Identify the blood parasite species.
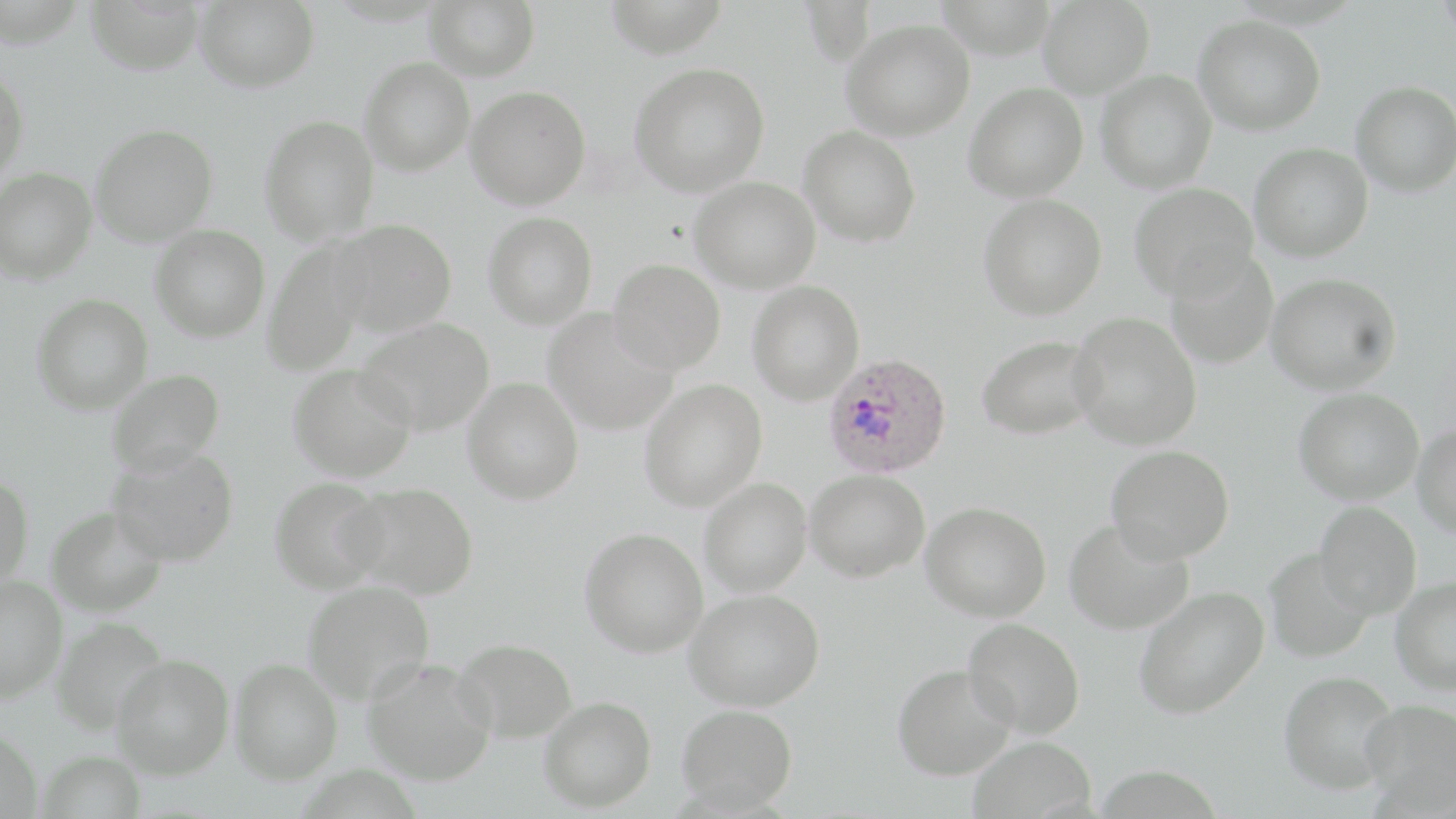
Plasmodium ovale.

Approximate bounding boxes as (x1,y1)-(x2,y2) corner pairs in pixels. Uninfected red blood cell locations: (85,0)-(206,75), (194,0)-(319,93), (425,0)-(540,81), (601,0)-(730,58), (1037,0)-(1154,98), (1194,15)-(1325,135), (841,19)-(974,140), (359,58)-(475,175), (629,62)-(770,197), (0,66)-(29,188), (1096,69)-(1217,193), (1351,80)-(1456,197), (964,82)-(1088,202), (465,85)-(591,210), (259,114)-(380,244), (90,123)-(218,246), (798,126)-(921,247), (1249,142)-(1373,262), (1,167)-(97,283), (689,176)-(821,293), (1129,182)-(1259,300), (978,194)-(1107,319), (483,212)-(598,329), (329,218)-(457,337), (150,224)-(270,342), (262,237)-(375,376), (1165,248)-(1278,369), (609,258)-(726,374), (1266,273)-(1401,394), (747,280)-(865,405), (31,293)-(153,414), (542,308)-(677,436), (1069,312)-(1202,449), (355,316)-(495,436), (976,334)-(1102,440), (288,362)-(417,482), (106,368)-(225,476), (463,377)-(583,504), (639,379)-(767,511), (1294,388)-(1424,504), (1412,424)-(1456,537), (1106,444)-(1234,563), (107,445)-(239,566), (805,469)-(930,582), (0,473)-(34,593), (269,477)-(390,593), (699,477)-(812,598), (344,483)-(479,599), (1314,500)-(1422,618), (921,501)-(1052,622), (46,505)-(168,618), (1064,518)-(1194,635), (580,527)-(708,658), (1264,548)-(1376,662), (0,574)-(67,704), (1390,576)-(1456,694), (303,578)-(436,705), (1133,584)-(1270,719), (686,588)-(825,711), (50,617)-(169,736), (963,618)-(1085,738), (453,638)-(577,743), (111,654)-(234,779), (362,656)-(496,785), (230,657)-(343,784), (892,663)-(1016,780), (1279,669)-(1402,794), (539,695)-(656,812), (1360,699)-(1456,811), (676,703)-(797,812), (0,727)-(42,819), (968,735)-(1096,819). Plasmodium ovale-infected red blood cell locations: (823,353)-(952,478). Optical microscopy. Image is 1456×819 pixels. Single field of view. May-Grünwald-Giemsa stain. Captured at 1000x magnification. Thin blood film.